Outline each Plasmodium falciparum parasite and classify it by life-cycle stage.
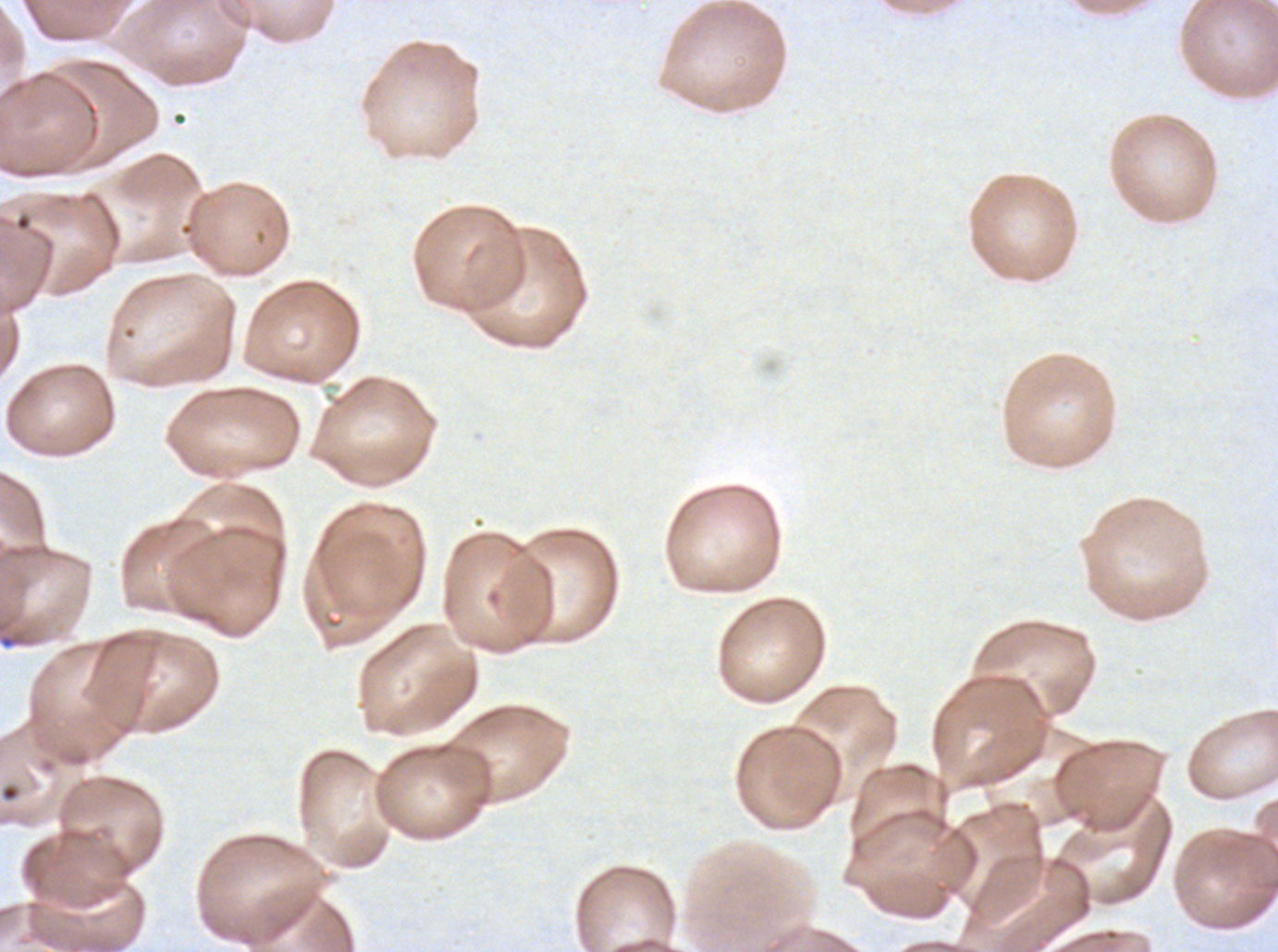

No rings, late-ring/early-trophozoite forms, mid trophozoites, late trophozoites, early schizonts, late schizonts, segmenters, or gametocytes observed.

notation = approximate bounding boxes as [x1, y1, x2, y2] in pixels
debris locations = [0, 784, 20, 802]
field of view = sub-image separated from a larger composite
image size = 1278×952 pixels
specimen = ex-vivo Plasmodium falciparum culture from a patient in The Gambia, grown for 24 to 48 hours
stain = Giemsa
preparation = thin blood film